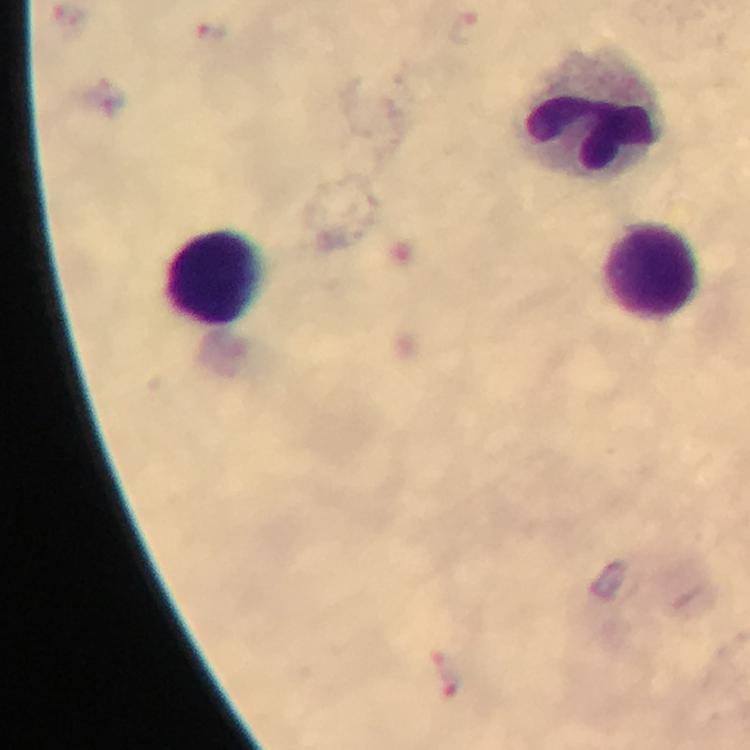 Approximate object centers, in pixels from the top-left corner. Leukocyte locations: (x=591, y=112), (x=651, y=270), (x=214, y=280). Malaria parasite locations: (x=440, y=659), (x=452, y=686). Image is 750×750 pixels. Immersion oil applied. Photographed through the microscope with a smartphone camera. Giemsa stain. Cropped region of a single field of view. At 100x magnification. Thick smear. From a malaria diagnostic workup.